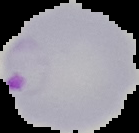
Summary:
  - Image size: 139×133 pixels
  - Preparation: thin blood smear
  - Image type: cell region segmented out of the field of view; surrounding area masked to black
  - Malaria status: parasitized